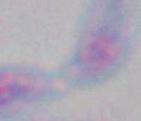

Summary:
  - Magnification: 1000x
  - Modality: photomicrograph
  - Identification: Toxoplasma gondii